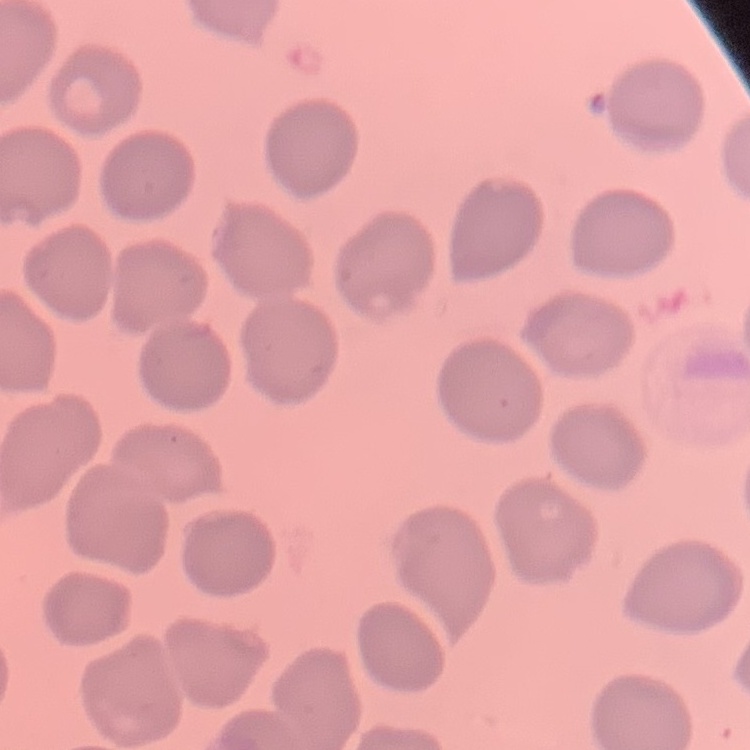 The erythrocytes show no rouleaux formation. Thin blood smear. One tile cut from a larger photomicrograph. Stained with either Field's or Giemsa.